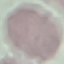

Summary:
  - Result: no malaria parasites seen
  - Stain: Giemsa
  - Preparation: thin blood smear
  - Image type: cell patch, automatically extracted from a larger field of view and resized to 64 × 64 pixels
  - Capture: smartphone camera at the microscope eyepiece